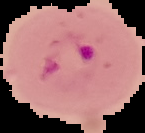

Summary:
  - Preparation: thin blood smear
  - Image type: segmented cell region with the area outside set to black
  - Malaria status: parasitized
  - Image size: 145×133 pixels